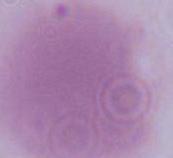

A red blood cell is seen. Micrograph. 1000x magnification.